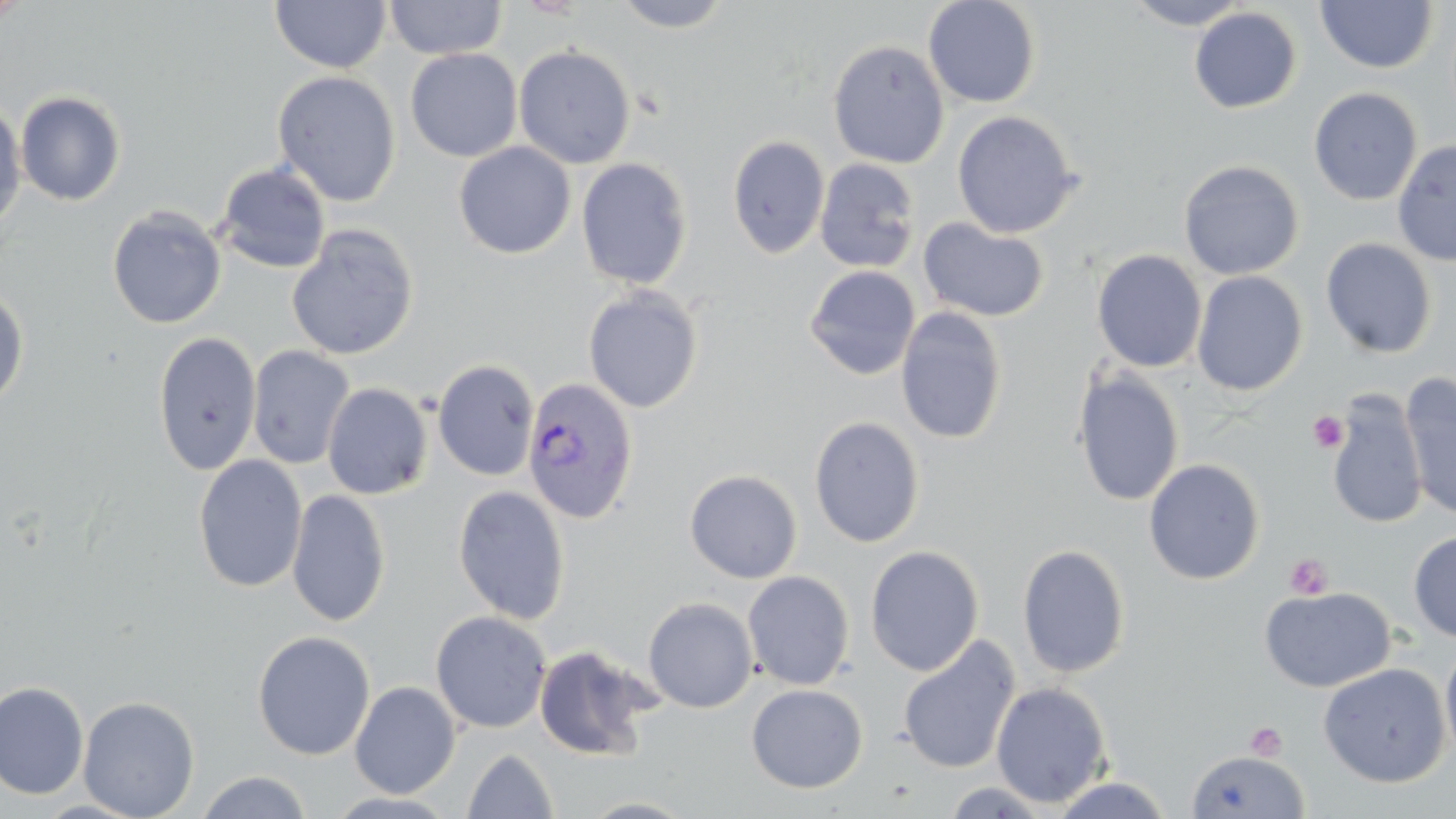 Approximate bounding boxes as (x1,y1)-(x2,y2) corner pairs in pixels. Uninfected red blood cell locations: (384,0)-(508,60), (611,0)-(736,33), (923,0)-(1041,108), (1124,0)-(1252,30), (270,1)-(391,74), (1315,1)-(1439,74), (1188,7)-(1302,113), (828,39)-(949,169), (514,45)-(636,169), (405,48)-(523,162), (272,70)-(401,207), (1308,86)-(1423,206), (15,91)-(127,206), (0,100)-(27,232), (951,111)-(1082,238), (726,135)-(830,259), (1393,140)-(1456,267), (454,142)-(576,259), (575,157)-(693,290), (814,158)-(922,273), (1178,159)-(1304,280), (214,162)-(332,274), (107,206)-(226,329), (918,217)-(1049,322), (286,225)-(420,361), (1320,238)-(1437,359), (1092,249)-(1208,372), (804,265)-(920,380), (1191,270)-(1308,396), (583,285)-(704,414), (0,286)-(29,412), (896,306)-(1009,444), (152,331)-(261,475), (247,345)-(355,469), (432,359)-(539,481), (1072,369)-(1185,507), (1399,374)-(1456,521), (321,382)-(434,499), (1327,391)-(1427,530), (809,416)-(925,548), (193,455)-(308,593), (1143,458)-(1265,585), (684,468)-(803,583), (452,484)-(570,625), (286,489)-(391,628), (1408,530)-(1456,643), (1016,543)-(1131,679), (864,545)-(984,676), (742,570)-(855,690), (1259,586)-(1396,693), (643,596)-(758,713), (430,610)-(552,734), (252,629)-(376,760), (897,635)-(1021,775), (1440,636)-(1456,768), (533,644)-(658,760), (1318,662)-(1450,787), (0,680)-(89,799), (350,680)-(461,798), (990,681)-(1113,807), (745,683)-(868,793), (78,696)-(200,818), (463,748)-(558,818), (1185,748)-(1311,818), (196,770)-(313,819), (1051,776)-(1174,818), (324,790)-(461,817). Plasmodium vivax-infected red blood cell locations: (522,377)-(639,524). Platelet locations: (1308,411)-(1348,453), (1285,553)-(1333,600), (1244,721)-(1288,761). Slide-level diagnosis: Plasmodium vivax. Thin blood smear. One field of a larger specimen. Light microscopy. May-Grünwald-Giemsa stain. Captured at 1000x magnification. Image is 1456×819 pixels.